Classify this cell by malaria status.
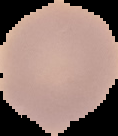
It is uninfected.

Summary:
  - Image size: 118×136 pixels
  - Image type: segmented cell region with the area outside set to black
  - Preparation: thin blood film